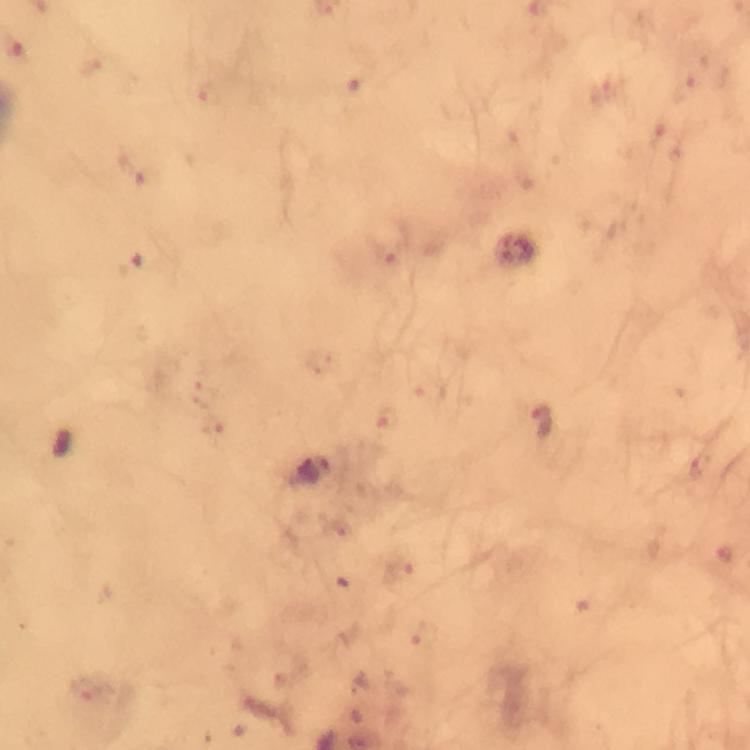

malaria parasite locations = approximate centers as [x, y] in pixels: [541, 424]
magnification = 100x
stain = Giemsa
capture = smartphone camera through the microscope
cropped from = a single field of view
preparation = thick blood film
image size = 750×750 pixels
context = from a malaria diagnostic workup
immersion oil = used